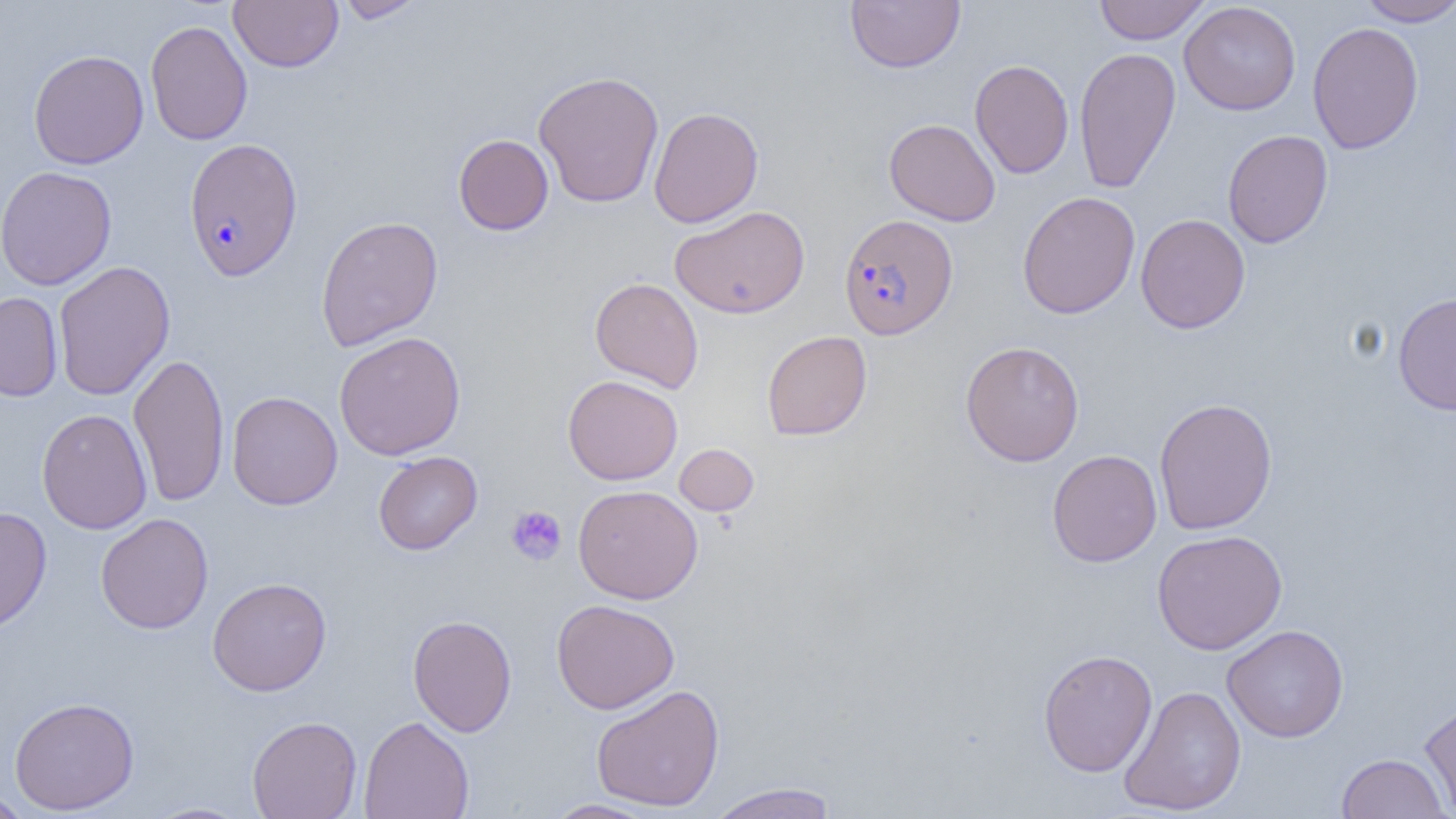

Approximate bounding boxes as (x1,y1)-(x2,y2) corner pairs in pixels. Plasmodium falciparum-infected red blood cell locations: (183,138)-(303,281), (838,214)-(958,340). Platelet locations: (506,505)-(567,566). Uninfected red blood cell locations: (229,0)-(343,72), (335,0)-(427,23), (845,0)-(966,73), (1094,0)-(1210,44), (1354,0)-(1456,26), (1179,2)-(1301,116), (145,20)-(253,145), (1307,22)-(1424,154), (1073,46)-(1182,195), (28,49)-(149,169), (969,59)-(1074,179), (533,70)-(664,208), (648,106)-(763,228), (884,118)-(1000,226), (1222,130)-(1333,248), (453,134)-(554,235), (0,165)-(116,290), (1017,191)-(1141,319), (670,205)-(810,319), (1135,214)-(1250,334), (315,215)-(444,352), (53,261)-(175,400), (590,277)-(704,393), (1393,291)-(1456,416), (0,292)-(63,401), (761,330)-(872,441), (334,331)-(466,460), (960,340)-(1085,467), (128,352)-(229,507), (562,375)-(683,485), (226,391)-(342,510), (1153,397)-(1278,535), (36,408)-(152,535), (674,443)-(759,516), (1047,449)-(1162,568), (373,451)-(483,554), (573,484)-(703,604), (0,506)-(52,634), (95,513)-(213,634), (1152,529)-(1288,654), (207,577)-(332,696), (551,599)-(679,714), (408,614)-(517,736), (1222,624)-(1349,742), (1038,649)-(1158,777), (591,684)-(725,812), (1118,685)-(1246,815), (9,696)-(139,815), (1419,698)-(1456,816), (247,715)-(362,819), (359,715)-(474,819), (1335,752)-(1451,819), (705,782)-(839,819), (1,790)-(35,818), (545,799)-(661,818), (142,802)-(254,819). Slide-level diagnosis: Plasmodium falciparum. Light microscopy. Single field of view. Thin blood film. Image is 1456×819 pixels. Captured at 1000x magnification.